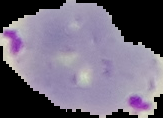
Summary:
  - Preparation: thin blood film
  - Result: malaria parasites detected
  - Image type: segmented cell region on a black background
  - Image size: 163×118 pixels